Identify the cell.
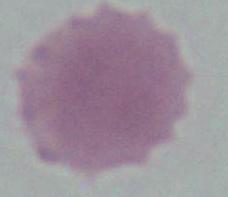

An erythrocyte.

Photomicrograph. 1000x magnification.